Identify the parasite.
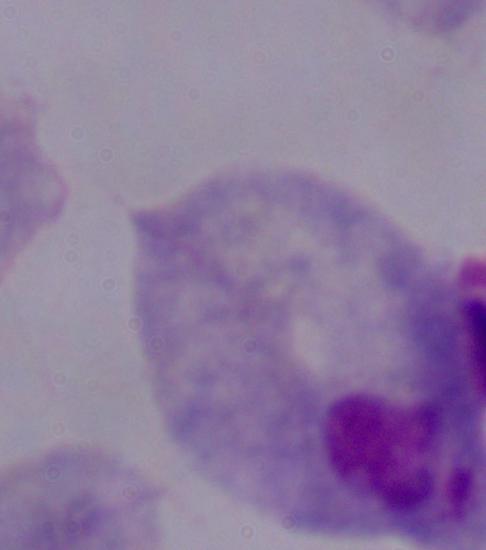
A trichomonad.

modality: micrograph
magnification: 1000x